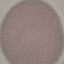
malaria status = uninfected
stain = Giemsa
capture = smartphone through the microscope eyepiece
image type = cell patch, automatically extracted from a larger field of view and resized to 64 × 64 pixels
preparation = thin smear